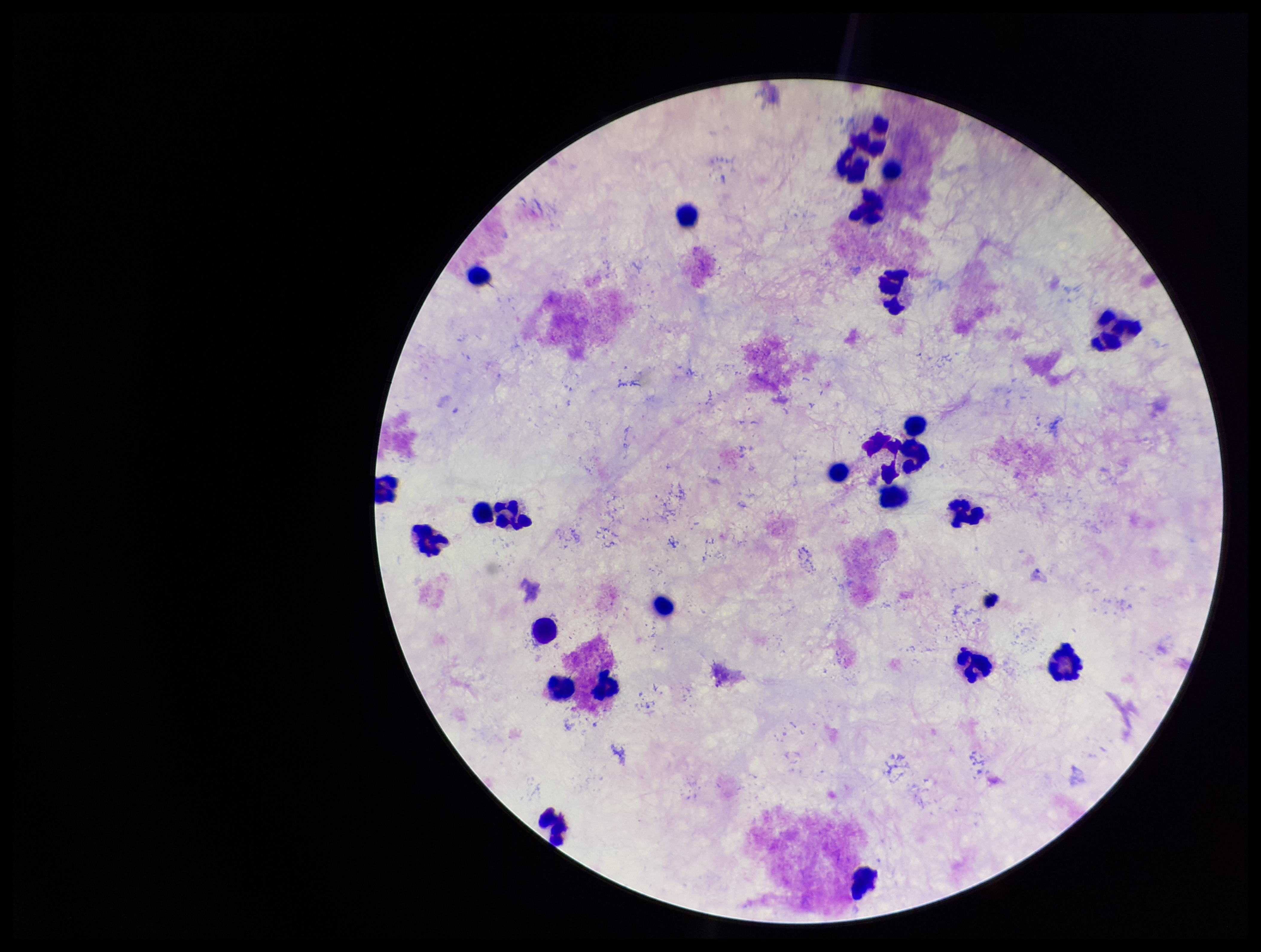

image size = 1261×952 pixels
capture = smartphone photograph through the microscope eyepiece
field of view = one from this slide
parasite count = 0
preparation = thick smear
leukocyte count = 23
stain = Giemsa
patient malaria status = negative
Plasmodium parasites = none detected